Find each parasitized red blood cell.
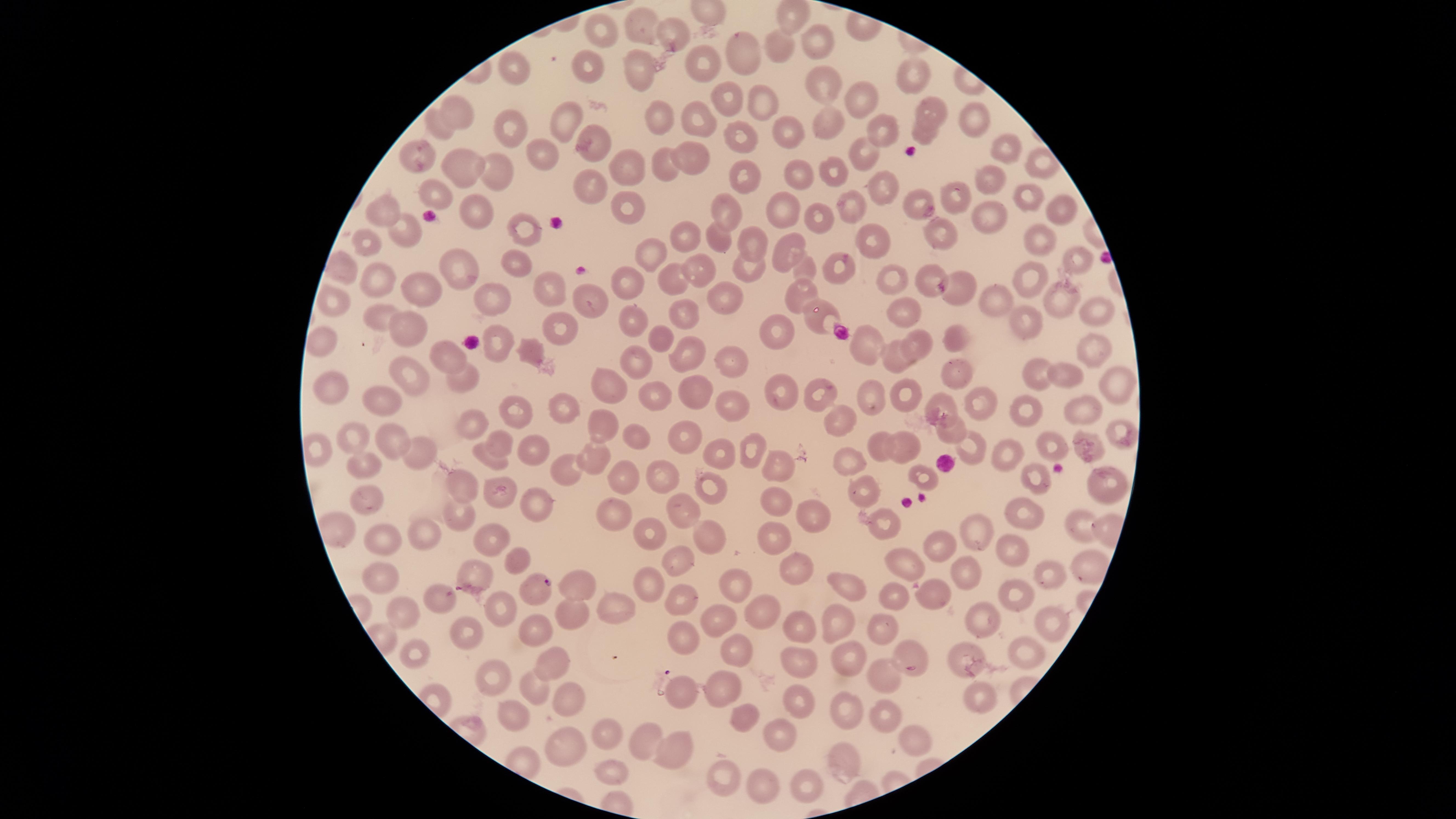

Approximate marker points as (x, y) in pixels.
Parasitized red blood cells: (542, 582).

visible region = circular
preparation = thin smear of blood
uninfected red blood cells = approximate marker points as (x, y) in pixels: (640, 30), (673, 30), (603, 33), (816, 41), (777, 44), (747, 55), (591, 65), (520, 67), (702, 67), (636, 68), (919, 73), (820, 87), (865, 97), (765, 100), (726, 102), (926, 108), (461, 113), (969, 114), (695, 116), (568, 117), (661, 118), (440, 121), (823, 125), (508, 126), (786, 126), (881, 132), (925, 133), (739, 134), (596, 144), (1005, 151), (419, 152), (864, 153), (694, 155), (542, 156), (663, 164), (460, 165), (631, 166), (1040, 166), (838, 168), (799, 170), (500, 172), (745, 179), (877, 183), (986, 184), (587, 185), (960, 194), (1021, 194), (436, 196), (852, 198), (913, 199), (621, 206), (730, 208), (387, 211), (474, 211), (777, 211), (1055, 211), (817, 214), (989, 216), (522, 229), (405, 230), (947, 232), (683, 236), (869, 238), (1042, 238), (718, 239), (370, 244), (754, 246), (782, 250), (650, 255), (1074, 256), (512, 261), (837, 262), (700, 265), (339, 266), (806, 266), (464, 268), (752, 270), (668, 274), (630, 275), (886, 278), (375, 279), (923, 279), (1033, 279), (550, 285), (421, 286), (961, 291), (338, 294), (719, 295), (796, 296), (995, 296), (493, 299), (1062, 300), (590, 303), (898, 309), (1090, 311), (690, 312), (380, 314), (634, 316), (817, 319), (1028, 321), (415, 326), (557, 326), (770, 330), (661, 332), (952, 335), (323, 341), (497, 341), (920, 344), (1088, 347), (867, 351), (447, 354), (682, 355), (894, 355), (637, 357), (732, 359), (954, 370), (1033, 374), (1067, 375), (461, 376), (416, 377), (330, 383), (1121, 383), (611, 385), (783, 389), (690, 391), (902, 392), (824, 393), (649, 398), (870, 400), (386, 403), (732, 403), (942, 404), (981, 404), (1087, 405), (566, 406), (1028, 407), (517, 413), (836, 414), (604, 416), (473, 418), (945, 427), (1120, 427), (685, 431), (350, 434), (393, 437), (636, 437), (1085, 438), (500, 440), (1050, 441), (755, 445), (877, 445), (973, 445), (908, 447), (317, 448), (540, 451), (419, 452), (722, 454), (1009, 454), (496, 460), (851, 460), (596, 461), (359, 464), (779, 465), (568, 467), (660, 472), (622, 473), (926, 473), (1032, 475), (705, 477), (462, 483), (1104, 485), (866, 494), (368, 495), (776, 496), (501, 497), (535, 499), (685, 506), (613, 507), (460, 508), (1024, 513), (808, 516), (884, 521), (1076, 524), (647, 529), (705, 529), (425, 532), (979, 532), (493, 534), (775, 540), (386, 544), (945, 546), (1015, 546), (902, 554), (678, 556), (520, 560), (789, 563), (475, 569), (1043, 570), (968, 572), (384, 579), (646, 579), (842, 581), (734, 584), (580, 589), (934, 593), (1017, 593), (892, 594), (437, 598), (678, 601), (497, 605), (617, 606), (402, 610), (574, 610), (763, 610), (1047, 615), (832, 616), (719, 619), (979, 620), (800, 624), (882, 625), (540, 629), (467, 635), (683, 639), (1030, 644), (413, 651), (550, 652), (736, 652), (910, 652), (849, 653), (960, 654), (795, 663), (497, 671), (886, 675), (721, 679), (532, 688), (682, 695), (978, 695), (571, 699), (795, 701), (846, 709), (741, 712), (512, 714), (883, 714), (606, 733), (782, 735), (645, 739), (916, 739), (669, 744), (565, 746), (844, 753), (608, 772), (727, 774), (765, 783), (805, 783)
stain = Giemsa
species = Plasmodium falciparum
image size = 1456×819 pixels
capture = smartphone photograph through the microscope eyepiece
field of view = single